Comment on the morphology of the erythrocytes.
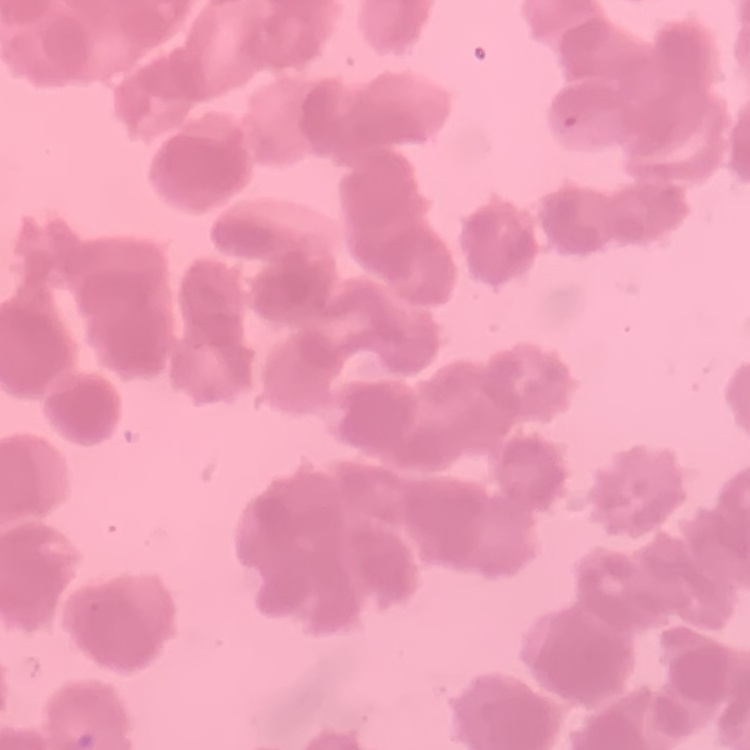

They show rouleaux formation.

preparation: thin peripheral smear
image_type: one tile cut from a larger photomicrograph
stain: Field's or Giemsa